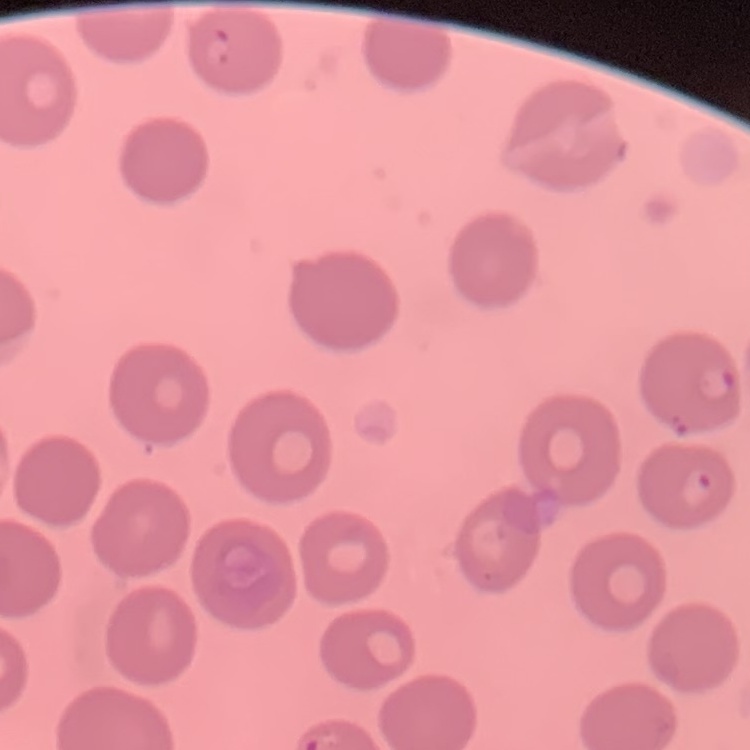

erythrocyte morphology = no rouleaux formation
stain = Field's or Giemsa
image type = one tile cut from a larger photomicrograph
preparation = thin blood smear